Classify the preparation.
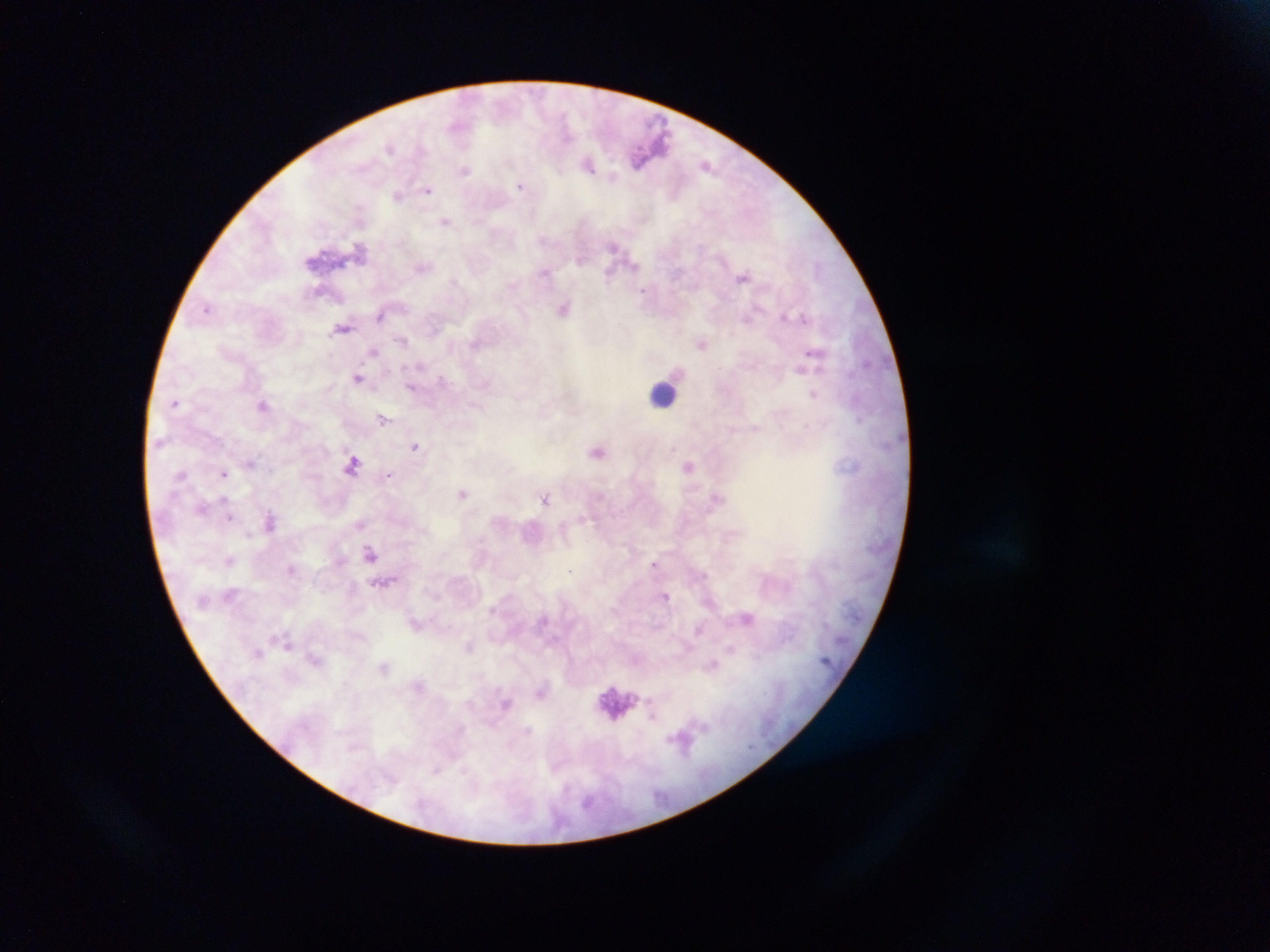

Thick blood film.

Approximate centers as [x, y] in pixels. Leukocyte locations: [662, 393], [615, 702]. Malaria parasite locations: [458, 125], [390, 147], [639, 156], [588, 164], [707, 166], [465, 169], [521, 186], [428, 189], [398, 194], [446, 221], [545, 271], [610, 273], [744, 277], [646, 290], [564, 307], [207, 308], [381, 316], [784, 317], [343, 327], [403, 340], [702, 343], [375, 351], [815, 355], [358, 378], [412, 386], [814, 394], [175, 401], [264, 405], [383, 418], [416, 447], [599, 450], [250, 463], [352, 463], [689, 465], [224, 473], [388, 474], [463, 493], [717, 497], [546, 498], [202, 508], [230, 517], [271, 521], [361, 525], [371, 554], [230, 559], [656, 565], [292, 569], [382, 583], [666, 597], [748, 618], [416, 624], [289, 644], [470, 646], [258, 652], [315, 659], [713, 664], [420, 685], [541, 692], [506, 703], [680, 738]. Image is 1270×952 pixels. Sample from Ghana. One field of view. Photographed through a microscope with a mobile-phone camera.